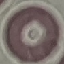

Result: no malaria parasites seen. Acquired by smartphone through the microscope eyepiece. Cell patch, automatically extracted from a larger field of view and resized to 64 × 64 pixels. Giemsa-stained preparation. Thin smear of blood.